Classify this cell by malaria status.
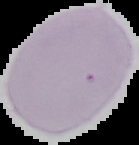
Uninfected.

From a thin blood smear. Image is 139×145 pixels. The area outside the segmented cell region is set to black.